Assess this cell for malaria.
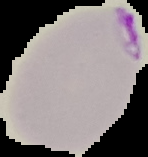
Parasitized.

{
  "image_size": "148×157 pixels",
  "image_type": "cell region segmented out of the field of view; surrounding area masked to black",
  "preparation": "thin blood film"
}